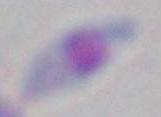 Photomicrograph. Toxoplasma gondii is shown. 1000x magnification.